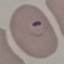
Summary:
  - Malaria status: parasitized
  - Stain: Giemsa
  - Image type: cell patch, automatically extracted from a larger field of view and resized to 64 × 64 pixels
  - Capture: smartphone through the microscope eyepiece
  - Preparation: thin blood film